Outline each Plasmodium ovale-infected red blood cell.
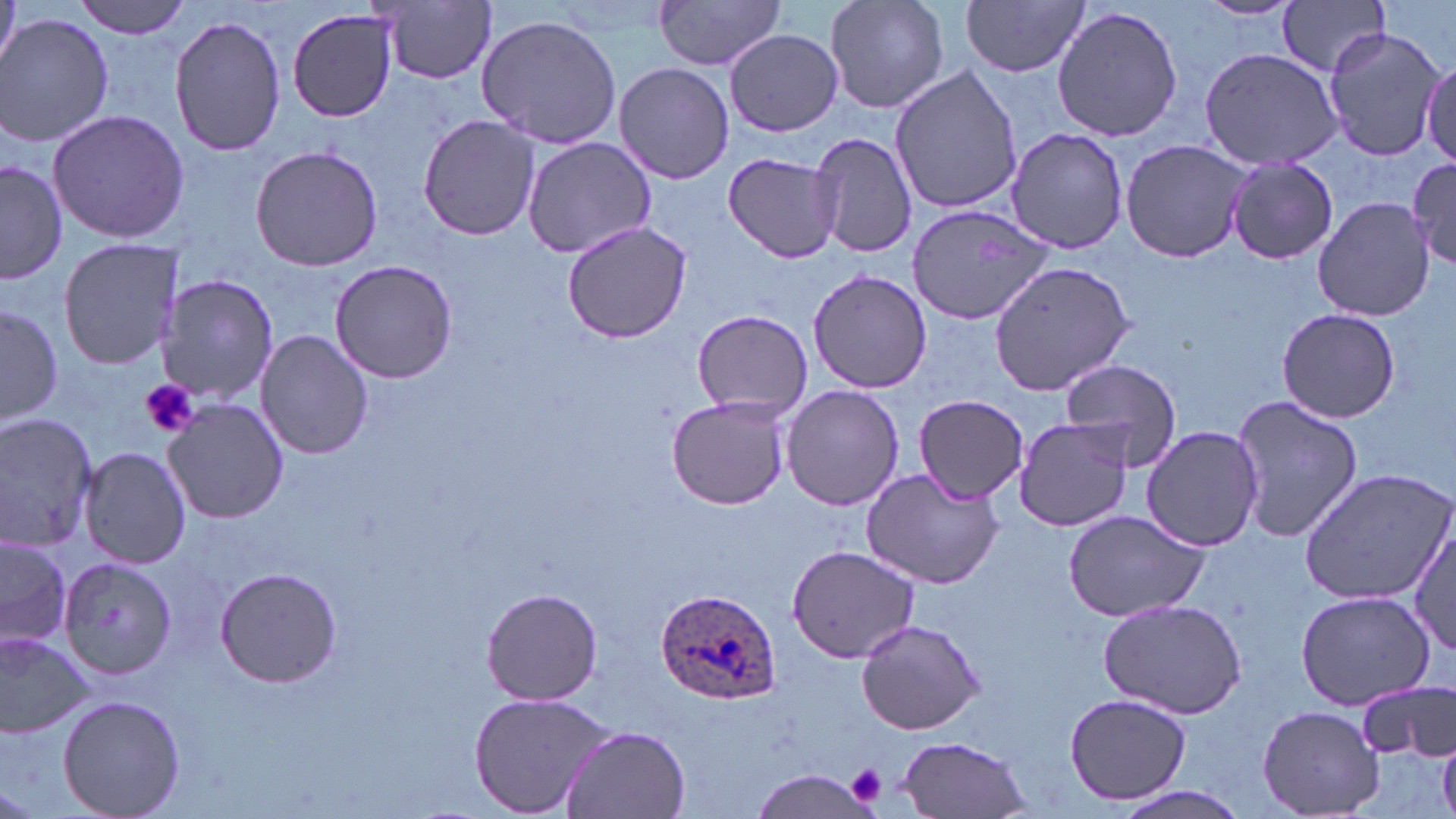

Approximate bounding boxes as (x1, y1, x2, y2) in pixels.
Plasmodium ovale-infected red blood cells: (655, 589, 781, 707).

slide-level diagnosis = Plasmodium ovale
modality = optical microscopy
magnification = 1000x
platelet locations = approximate bounding boxes as (x1, y1, x2, y2) in pixels: (140, 378, 199, 438), (847, 764, 886, 802)
field of view = single
stain = May-Grünwald-Giemsa
uninfected red blood cell locations = approximate bounding boxes as (x1, y1, x2, y2) in pixels: (71, 0, 194, 39), (654, 0, 787, 71), (823, 0, 949, 115), (962, 0, 1090, 77), (1196, 0, 1302, 21), (1278, 0, 1391, 77), (0, 1, 20, 73), (376, 1, 501, 85), (1052, 5, 1184, 142), (287, 7, 400, 124), (169, 14, 287, 160), (1, 15, 115, 148), (476, 15, 624, 150), (1321, 24, 1447, 162), (725, 30, 843, 136), (1196, 46, 1344, 172), (1422, 54, 1456, 165), (613, 62, 734, 184), (888, 64, 1023, 215), (46, 109, 190, 244), (418, 115, 542, 242), (1006, 127, 1129, 254), (809, 130, 917, 259), (522, 136, 661, 261), (1118, 138, 1255, 266), (249, 145, 383, 272), (722, 150, 844, 264), (1408, 155, 1456, 270), (0, 159, 68, 285), (1225, 159, 1338, 265), (1312, 196, 1435, 320), (908, 204, 1056, 325), (560, 219, 694, 344), (58, 237, 183, 370), (330, 258, 457, 385), (988, 259, 1137, 394), (807, 268, 932, 393), (158, 275, 277, 405), (0, 302, 63, 426), (1275, 306, 1401, 424), (691, 309, 813, 419), (256, 328, 373, 461), (1059, 361, 1183, 469), (781, 384, 904, 511), (1229, 393, 1363, 545), (912, 394, 1028, 501), (667, 395, 790, 511), (163, 399, 291, 523), (0, 413, 99, 554), (1012, 415, 1136, 532), (1140, 426, 1265, 551), (78, 445, 189, 569), (1297, 467, 1456, 605), (862, 469, 1004, 590), (1060, 505, 1211, 625), (1407, 523, 1456, 656), (0, 534, 73, 650), (786, 543, 921, 664), (59, 557, 177, 679), (213, 568, 341, 688), (483, 587, 603, 705), (1297, 588, 1437, 710), (1099, 597, 1248, 718), (853, 616, 986, 736), (0, 631, 93, 738), (1357, 679, 1456, 762), (466, 690, 619, 818), (1065, 692, 1191, 807), (57, 695, 186, 819), (1258, 704, 1387, 817), (561, 724, 694, 817), (894, 735, 1034, 818), (752, 767, 879, 817), (1102, 785, 1254, 819)
image size = 1456×819 pixels
preparation = thin blood smear